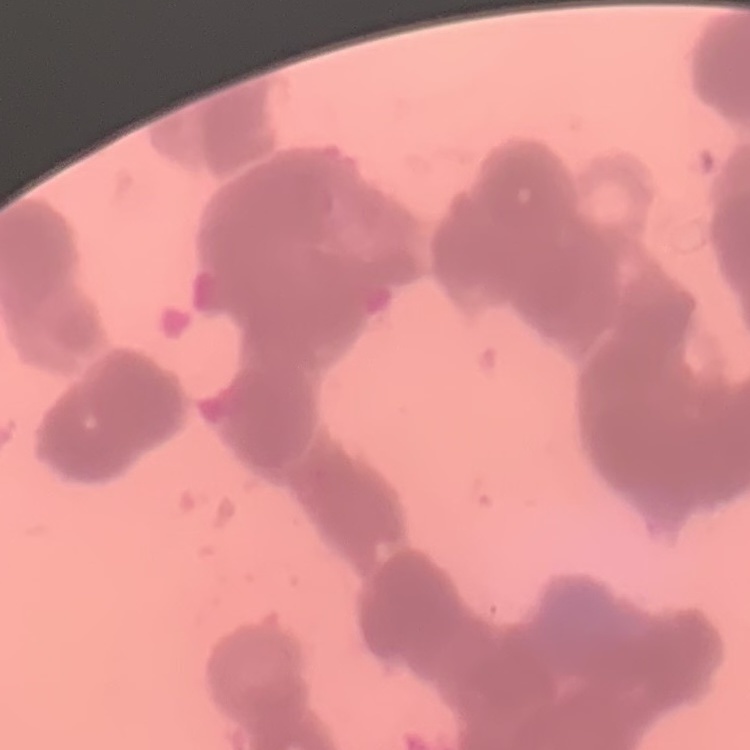
Summary:
  - Erythrocyte morphology: rouleaux formation
  - Image type: square crop of a larger photomicrograph
  - Preparation: thin peripheral smear
  - Stain: Field's or Giemsa